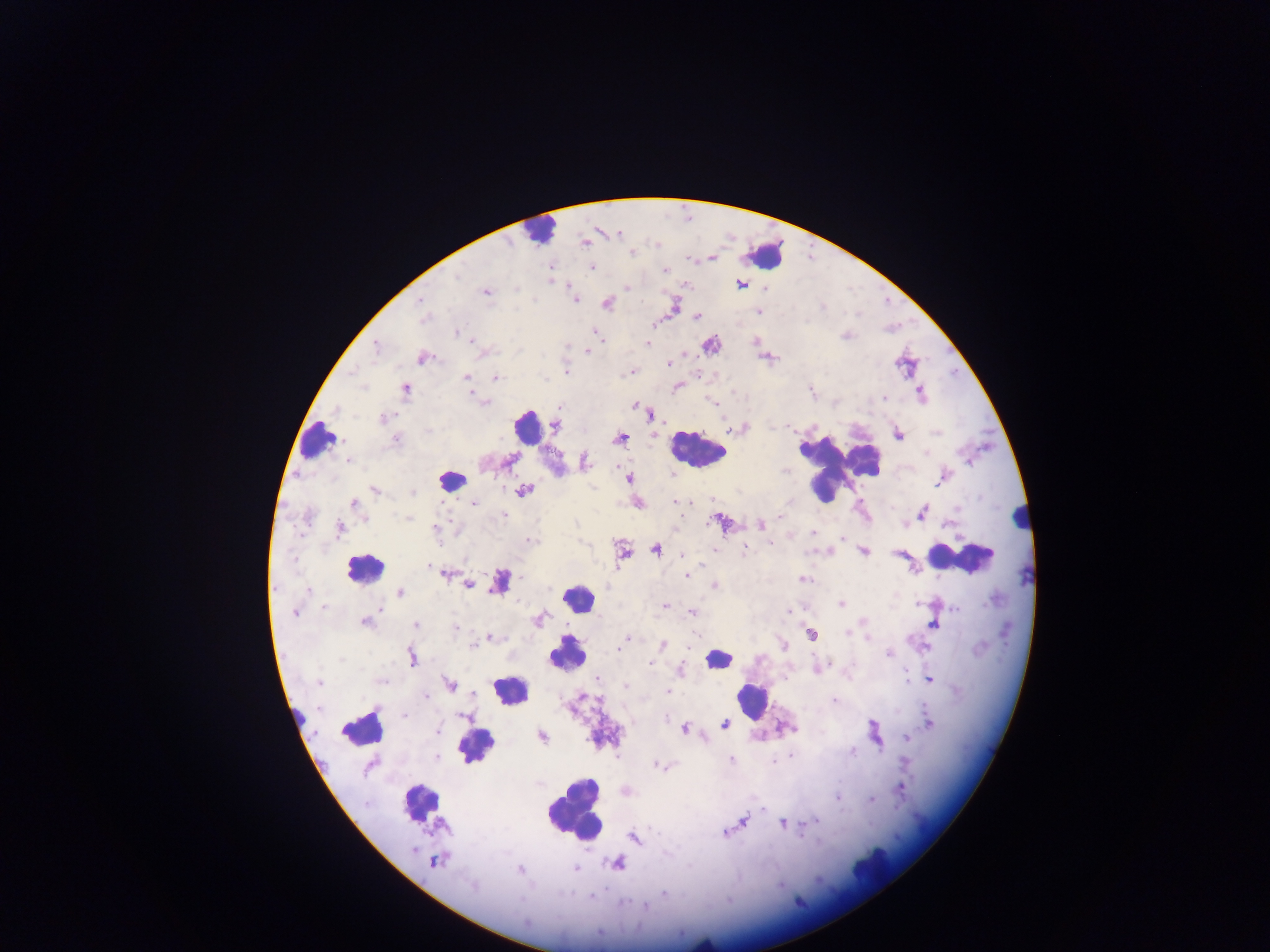

Approximate centers as {x, y} in pixels. Leukocyte locations: {536, 230}, {765, 256}, {528, 426}, {318, 441}, {696, 450}, {839, 464}, {450, 480}, {1020, 517}, {960, 558}, {364, 567}, {500, 588}, {578, 602}, {567, 653}, {717, 660}, {511, 689}, {751, 700}, {297, 713}, {362, 727}, {477, 746}, {421, 801}, {575, 811}, {871, 868}, {702, 942}. Plasmodium parasite locations: {618, 233}, {584, 243}, {631, 251}, {711, 257}, {591, 266}, {665, 271}, {552, 281}, {742, 284}, {684, 285}, {626, 287}, {765, 288}, {486, 291}, {575, 299}, {419, 300}, {606, 302}, {674, 306}, {759, 311}, {696, 316}, {424, 318}, {456, 332}, {594, 332}, {599, 338}, {756, 341}, {646, 344}, {710, 344}, {375, 347}, {587, 351}, {767, 356}, {423, 357}, {669, 362}, {565, 370}, {632, 372}, {465, 376}, {495, 378}, {677, 386}, {405, 389}, {920, 393}, {474, 397}, {884, 400}, {484, 401}, {559, 405}, {635, 405}, {641, 409}, {650, 413}, {383, 418}, {555, 425}, {727, 427}, {898, 433}, {620, 438}, {395, 439}, {508, 459}, {349, 460}, {584, 462}, {629, 478}, {375, 490}, {523, 490}, {473, 502}, {676, 502}, {353, 503}, {637, 503}, {922, 513}, {504, 514}, {408, 518}, {722, 522}, {759, 525}, {339, 528}, {434, 529}, {813, 533}, {845, 537}, {529, 540}, {772, 542}, {744, 547}, {713, 549}, {655, 550}, {830, 550}, {862, 550}, {621, 551}, {900, 553}, {429, 566}, {444, 573}, {686, 575}, {804, 579}, {467, 584}, {713, 585}, {308, 591}, {400, 592}, {841, 604}, {322, 606}, {664, 606}, {378, 607}, {294, 612}, {693, 612}, {539, 620}, {364, 621}, {416, 624}, {933, 624}, {845, 632}, {811, 634}, {490, 637}, {628, 639}, {868, 639}, {621, 643}, {471, 645}, {662, 645}, {782, 645}, {889, 653}, {411, 656}, {651, 663}, {818, 667}, {680, 670}, {928, 679}, {598, 680}, {318, 683}, {449, 685}, {668, 692}, {473, 694}, {426, 695}, {834, 701}, {404, 715}, {929, 723}, {724, 724}, {684, 727}, {438, 731}, {874, 734}, {541, 736}, {906, 738}, {852, 751}, {436, 756}, {730, 760}, {661, 766}, {899, 789}, {624, 791}, {837, 797}, {870, 799}, {742, 822}, {782, 823}, {724, 833}, {634, 838}, {436, 860}, {617, 863}, {575, 867}, {519, 869}, {663, 892}, {645, 907}. One field of view. Collected in Ghana. Image is 1270×952 pixels. Thick blood smear. Photographed through a microscope with a mobile-phone camera.